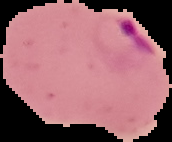

{
  "image_type": "segmented cell region with the area outside set to black",
  "image_size": "172×142 pixels",
  "malaria_status": "parasitized",
  "preparation": "thin blood smear"
}